State which parasite is depicted.
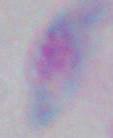
Toxoplasma gondii.

Summary:
  - Magnification: 1000x
  - Modality: photomicrograph